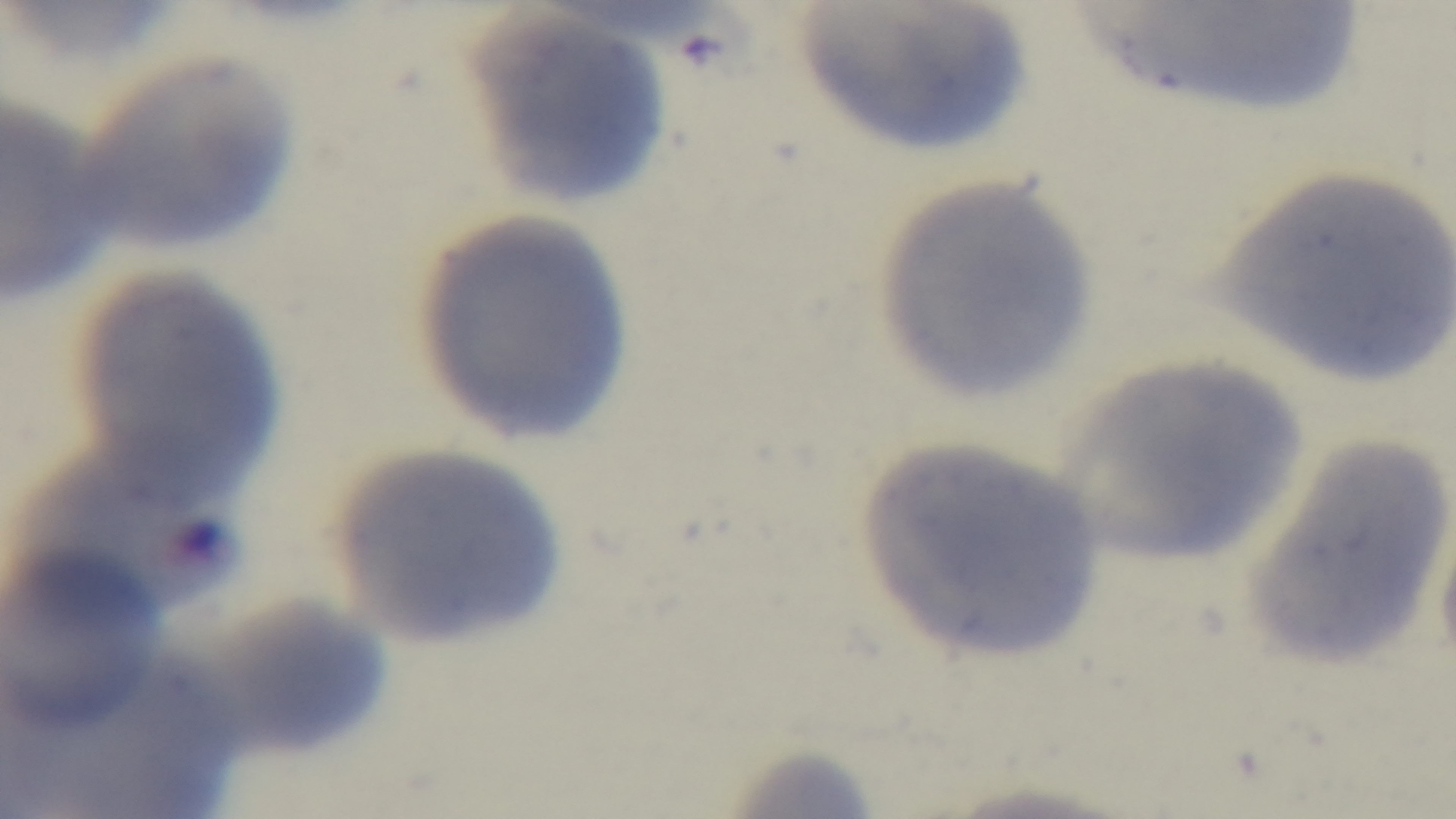

capture: mounted 4K digital camera
objective: 100x oil immersion
malaria_status: uninfected
stain: Giemsa
field_of_view: one from the slide
modality: light microscopy
preparation: thin